Name the parasite shown.
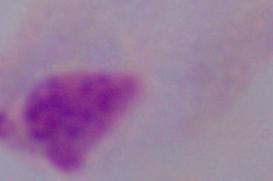
This is a trichomonad.

Summary:
  - Magnification: 1000x
  - Modality: micrograph